Locate and identify every blood parasite.
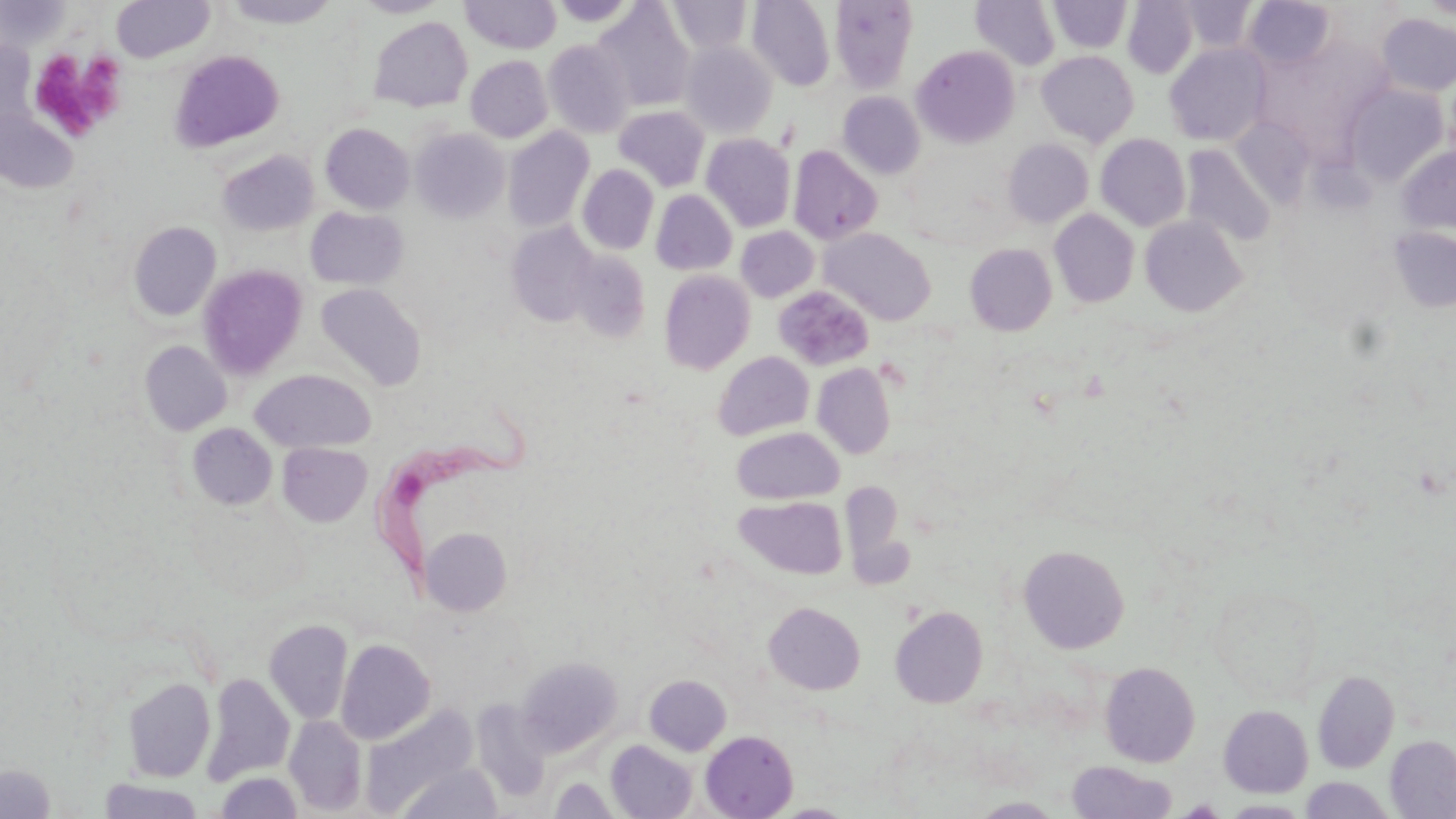
Approximate bounding boxes as (x1,y1)-(x2,y2) corner pairs in pixels.
Trypanosoma brucei: (378,397)-(544,577).
No Plasmodium falciparum, Plasmodium ovale, Plasmodium malariae, Plasmodium vivax, or Babesia divergens observed.

Summary:
  - Platelet locations: (27,49)-(127,142)
  - Uninfected red blood cell locations: (111,0)-(215,63), (352,0)-(452,17), (460,0)-(562,54), (667,0)-(753,54), (747,0)-(836,91), (830,0)-(917,93), (1048,0)-(1132,53), (1178,0)-(1258,54), (1244,0)-(1337,69), (0,1)-(69,52), (221,1)-(340,29), (550,1)-(640,27), (971,1)-(1060,70), (1123,1)-(1198,77), (593,2)-(695,111), (1376,13)-(1456,97), (368,17)-(473,112), (0,40)-(35,137), (543,40)-(634,138), (681,41)-(777,139), (1165,43)-(1270,146), (912,45)-(1019,148), (169,50)-(285,153), (1037,51)-(1139,147), (465,55)-(552,143), (1343,82)-(1449,186), (838,92)-(925,179), (614,106)-(710,191), (0,108)-(78,194), (1230,118)-(1313,206), (320,123)-(414,214), (503,127)-(594,233), (411,128)-(510,222), (702,134)-(796,232), (1096,134)-(1191,231), (1003,138)-(1093,227), (1181,145)-(1277,248), (789,146)-(883,245), (1397,146)-(1456,234), (217,150)-(318,236), (577,164)-(659,254), (651,190)-(737,275), (305,207)-(409,290), (1049,209)-(1140,308), (1140,216)-(1247,317), (129,220)-(221,321), (506,222)-(599,326), (736,226)-(819,302), (1387,226)-(1456,313), (820,228)-(936,326), (965,243)-(1057,335), (569,250)-(651,343), (198,264)-(308,378), (659,270)-(755,374), (316,283)-(426,391), (774,286)-(874,371), (139,340)-(231,435), (712,352)-(814,441), (812,363)-(895,458), (250,369)-(376,453), (188,423)-(277,510), (732,427)-(843,504), (277,442)-(372,527), (735,495)-(847,580), (419,526)-(512,615), (1018,544)-(1129,653), (1206,581)-(1325,703), (764,602)-(865,695), (891,605)-(988,707), (263,618)-(353,726), (336,638)-(435,744), (517,656)-(623,756), (1100,661)-(1200,767), (1312,669)-(1399,773), (200,672)-(295,786), (644,674)-(731,755), (123,677)-(215,782), (472,699)-(552,801), (1218,704)-(1313,797), (362,705)-(479,814), (284,715)-(367,815), (700,730)-(798,818), (1385,735)-(1456,818), (606,740)-(697,819), (1066,760)-(1177,818), (399,762)-(502,819), (0,763)-(56,819), (216,772)-(302,818), (1300,776)-(1395,818), (549,777)-(622,818), (96,778)-(205,818), (971,796)-(1064,817), (1221,800)-(1311,817), (773,802)-(855,817)
  - Slide-level diagnosis: Trypanosoma brucei
  - Magnification: 1000x
  - Modality: light microscopy
  - Stain: May-Grünwald-Giemsa
  - Preparation: thin blood smear
  - Image size: 1456×819 pixels
  - Field of view: one of a larger specimen